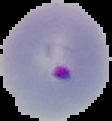
Cell region segmented out of the field of view; the surrounding area is masked to black. Malaria status: parasitized. Image is 112×121 pixels. From a thin blood film.